Locate every Plasmodium falciparum-infected red blood cell.
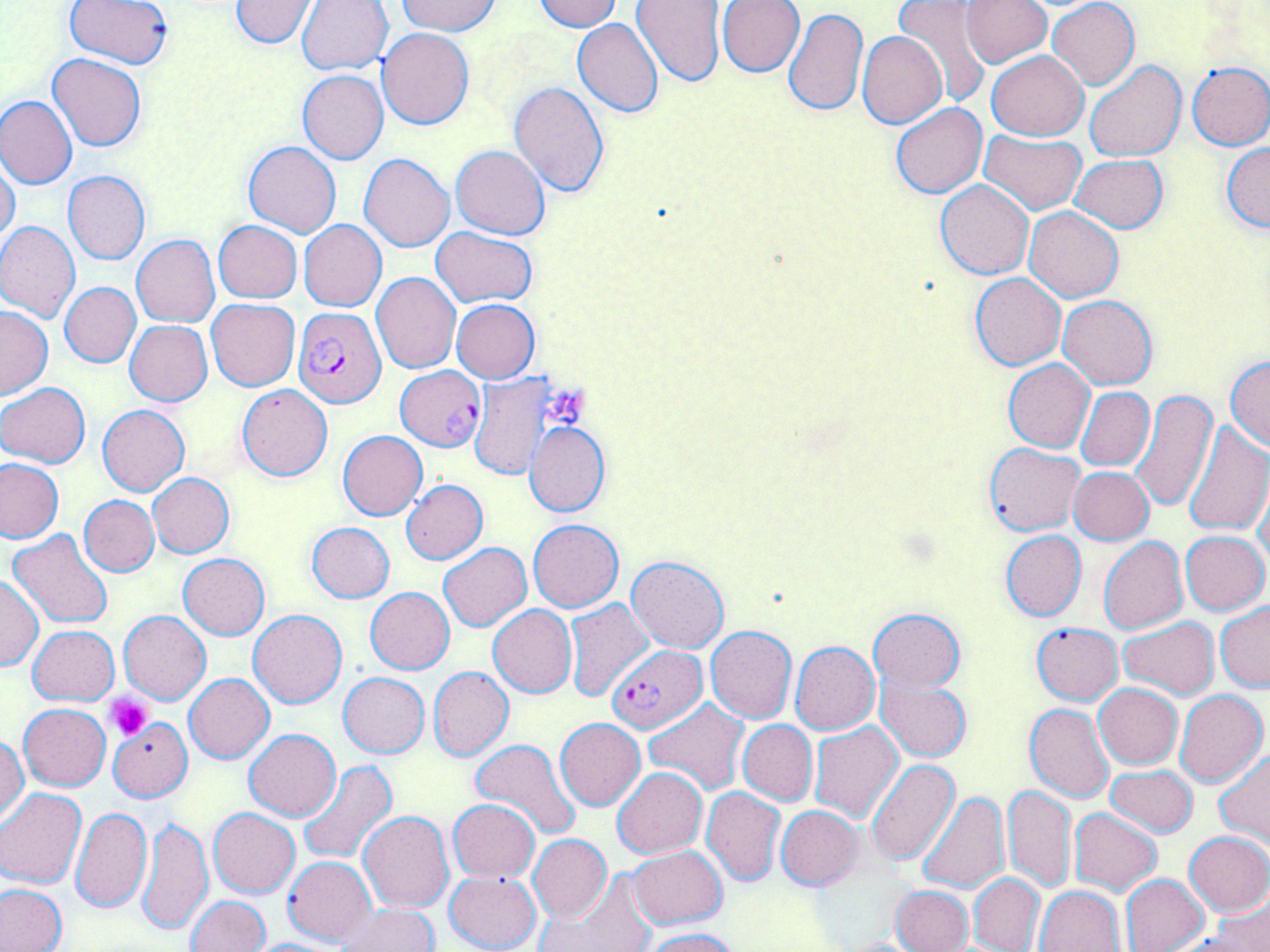
Approximate bounding boxes as (x1,y1)-(x2,y2) corner pairs in pixels.
Plasmodium falciparum-infected red blood cells: (293,307)-(387,409), (394,366)-(486,450), (608,645)-(706,732).

Uninfected red blood cell locations: (64,0)-(172,69), (229,0)-(319,49), (296,0)-(394,76), (397,0)-(500,36), (532,0)-(621,32), (716,0)-(805,77), (960,0)-(1050,69), (1047,0)-(1140,89), (632,1)-(727,87), (895,2)-(990,105), (783,8)-(867,117), (571,18)-(664,117), (377,28)-(474,129), (858,31)-(946,128), (986,50)-(1088,141), (48,53)-(146,152), (1085,61)-(1186,161), (1185,61)-(1270,150), (297,70)-(389,164), (508,81)-(610,196), (0,95)-(78,189), (891,102)-(987,199), (981,131)-(1086,214), (243,140)-(341,237), (1222,142)-(1270,232), (451,144)-(550,240), (359,153)-(455,252), (1070,155)-(1168,233), (0,160)-(20,245), (64,171)-(150,264), (935,180)-(1033,280), (1024,205)-(1123,303), (213,220)-(302,303), (299,220)-(388,312), (1,222)-(80,323), (431,227)-(536,307), (132,235)-(221,327), (372,272)-(461,372), (970,272)-(1066,371), (59,282)-(141,367), (1058,295)-(1157,390), (206,299)-(299,390), (451,300)-(540,383), (0,307)-(52,399), (124,320)-(213,406), (1225,355)-(1270,451), (1003,359)-(1095,453), (470,373)-(555,483), (0,382)-(91,469), (236,384)-(332,481), (1076,387)-(1154,471), (1128,387)-(1217,512), (97,405)-(190,495), (1182,421)-(1270,536), (526,422)-(610,517), (337,431)-(428,519), (984,443)-(1084,535), (0,458)-(66,544), (1069,466)-(1155,545), (148,473)-(236,558), (1256,474)-(1270,571), (401,480)-(488,563), (80,489)-(236,568), (79,495)-(159,577), (528,520)-(623,613), (306,522)-(395,603), (1000,530)-(1086,621), (1181,530)-(1269,614), (8,531)-(112,628), (1098,537)-(1188,634), (439,543)-(531,630), (179,554)-(270,640), (626,556)-(729,654), (0,575)-(43,670), (365,587)-(455,674), (563,598)-(653,701), (1216,602)-(1270,692), (487,605)-(577,698), (868,607)-(965,692), (249,609)-(346,708), (120,610)-(211,704), (1119,617)-(1220,700), (1031,621)-(1123,705), (28,626)-(119,704), (705,626)-(796,722), (791,641)-(880,735), (430,666)-(513,761), (338,672)-(429,758), (184,674)-(274,763), (876,675)-(972,762), (1094,683)-(1182,768), (1174,689)-(1269,788), (645,698)-(749,797), (1025,703)-(1114,803), (18,704)-(111,791), (108,717)-(191,801), (555,717)-(645,811), (738,720)-(817,805), (809,722)-(905,825), (244,729)-(340,821), (0,735)-(28,824), (471,739)-(581,840), (1216,751)-(1270,849), (296,760)-(398,864), (866,760)-(960,866), (1105,765)-(1198,837), (613,768)-(708,860), (1003,785)-(1077,893), (702,787)-(786,886), (0,788)-(87,888), (917,792)-(1008,894), (448,799)-(539,882), (776,805)-(862,888), (71,807)-(152,915), (208,808)-(301,898), (1070,808)-(1161,895), (359,811)-(454,912), (138,815)-(213,936), (1185,831)-(1268,917), (528,834)-(611,924), (627,845)-(726,928), (282,855)-(375,947), (444,870)-(542,952), (549,870)-(657,952), (969,874)-(1044,952), (1120,874)-(1209,952), (0,884)-(68,951), (890,885)-(973,952), (1035,885)-(1126,952), (1210,892)-(1270,952), (185,896)-(269,952), (336,904)-(438,952), (641,928)-(741,952), (241,938)-(345,952). Platelet locations: (547,384)-(590,429), (106,696)-(153,740). Slide-level diagnosis: Plasmodium falciparum. Captured at 1000x magnification. Image is 1270×952 pixels. May-Grünwald-Giemsa-stained preparation. Light microscopy. Thin blood film. Single field of view.